Assess for malaria.
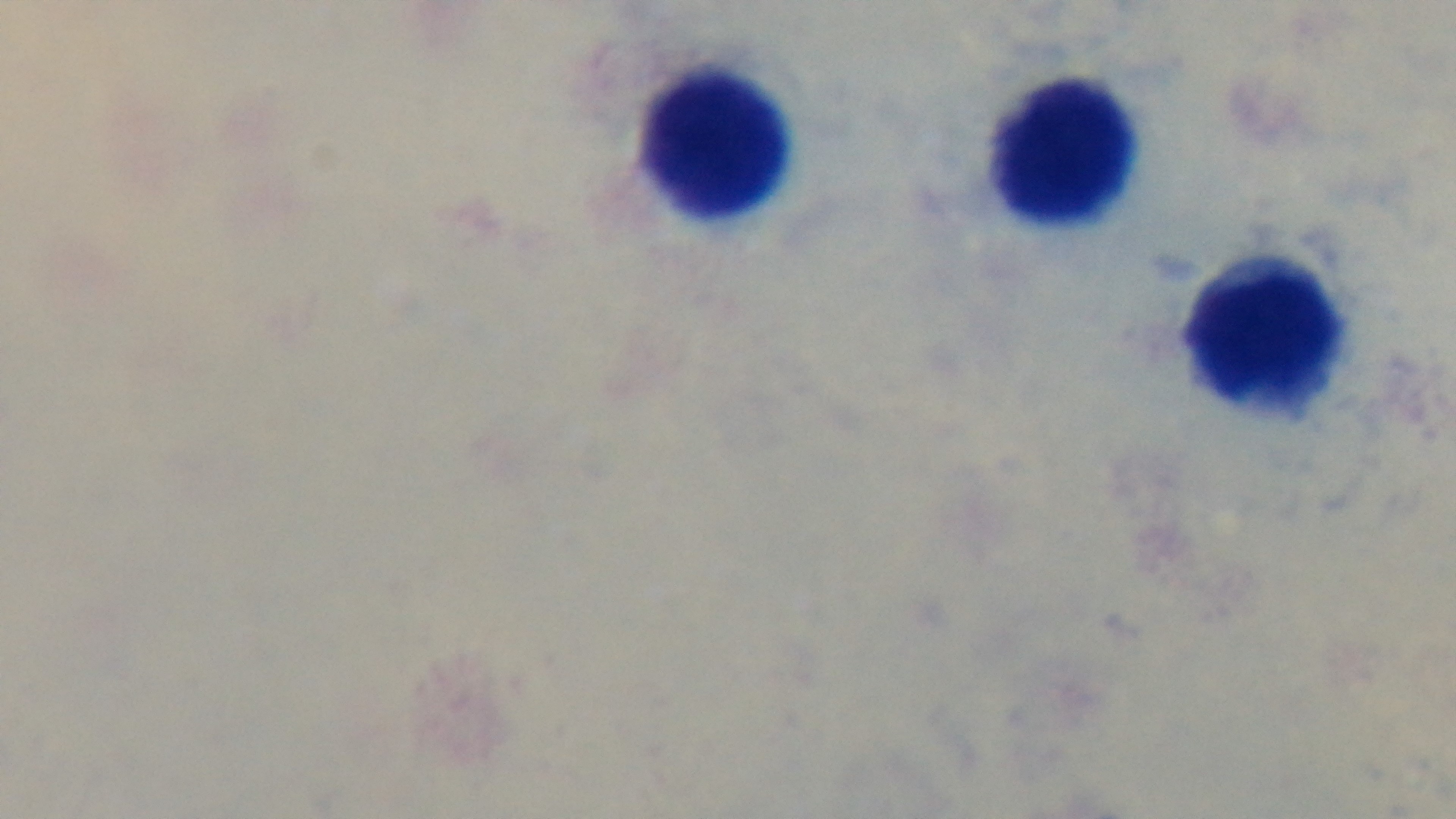

Uninfected.

{
  "preparation": "thick",
  "field_of_view": "one from the slide",
  "stain": "Giemsa",
  "modality": "light microscopy",
  "capture": "mounted 4K digital camera",
  "objective": "100x oil immersion"
}